Assess the morphology of the erythrocytes.
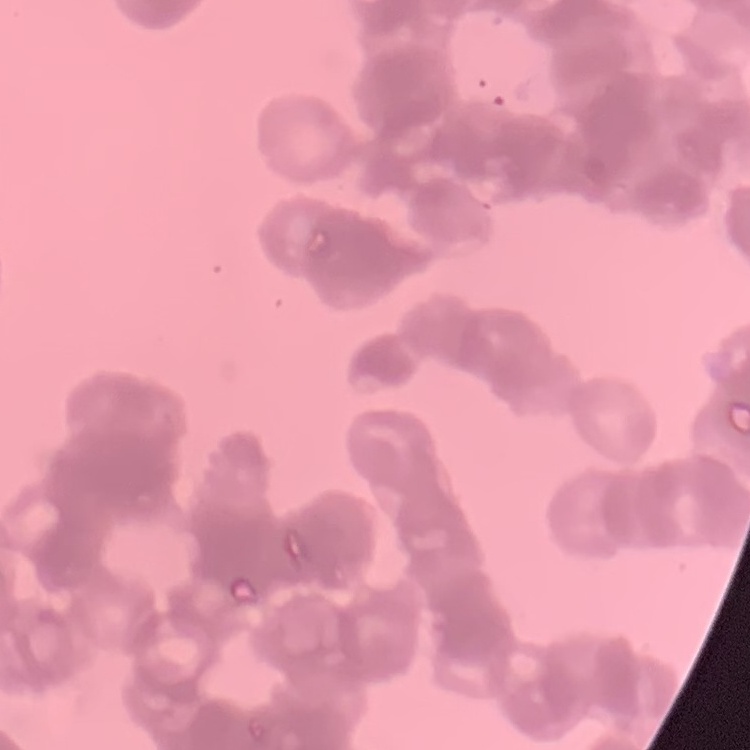

Rouleaux formation.

stain = Field's or Giemsa
preparation = thin blood smear
image type = one tile cut from a larger photomicrograph